Classify this cell by malaria status.
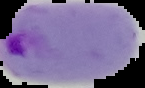

It is parasitized.

Summary:
  - Image size: 145×88 pixels
  - Image type: segmented cell region on a black background
  - Preparation: thin blood film